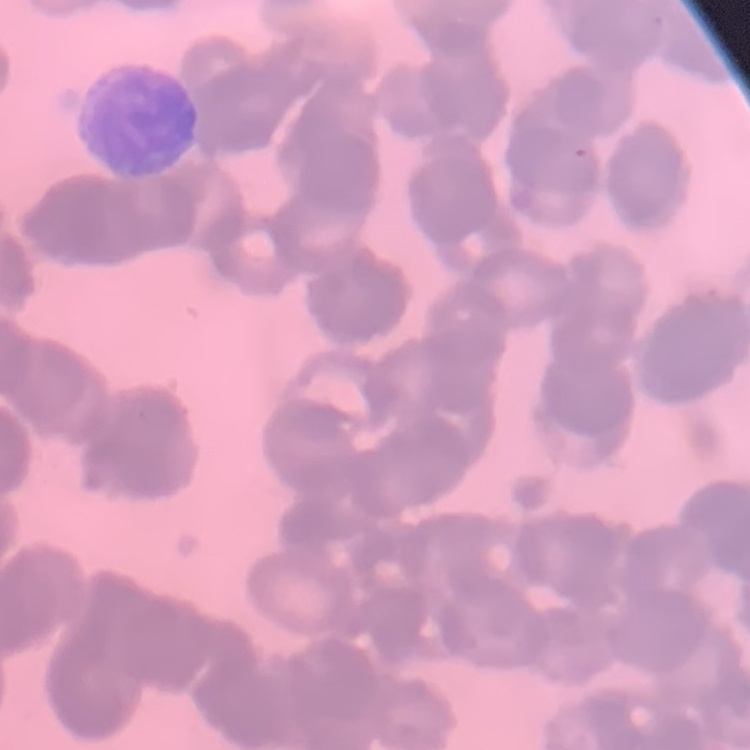

red_blood_cell_morphology: rouleaux formation
image_type: one tile cut from a larger photomicrograph
stain: Field's or Giemsa
preparation: thin blood smear